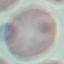
Malaria status: uninfected. Thin blood smear. Acquired by smartphone through the microscope eyepiece. Giemsa stain. Automatically extracted cell patch, resized to 64 × 64 pixels.